State the blood parasite species.
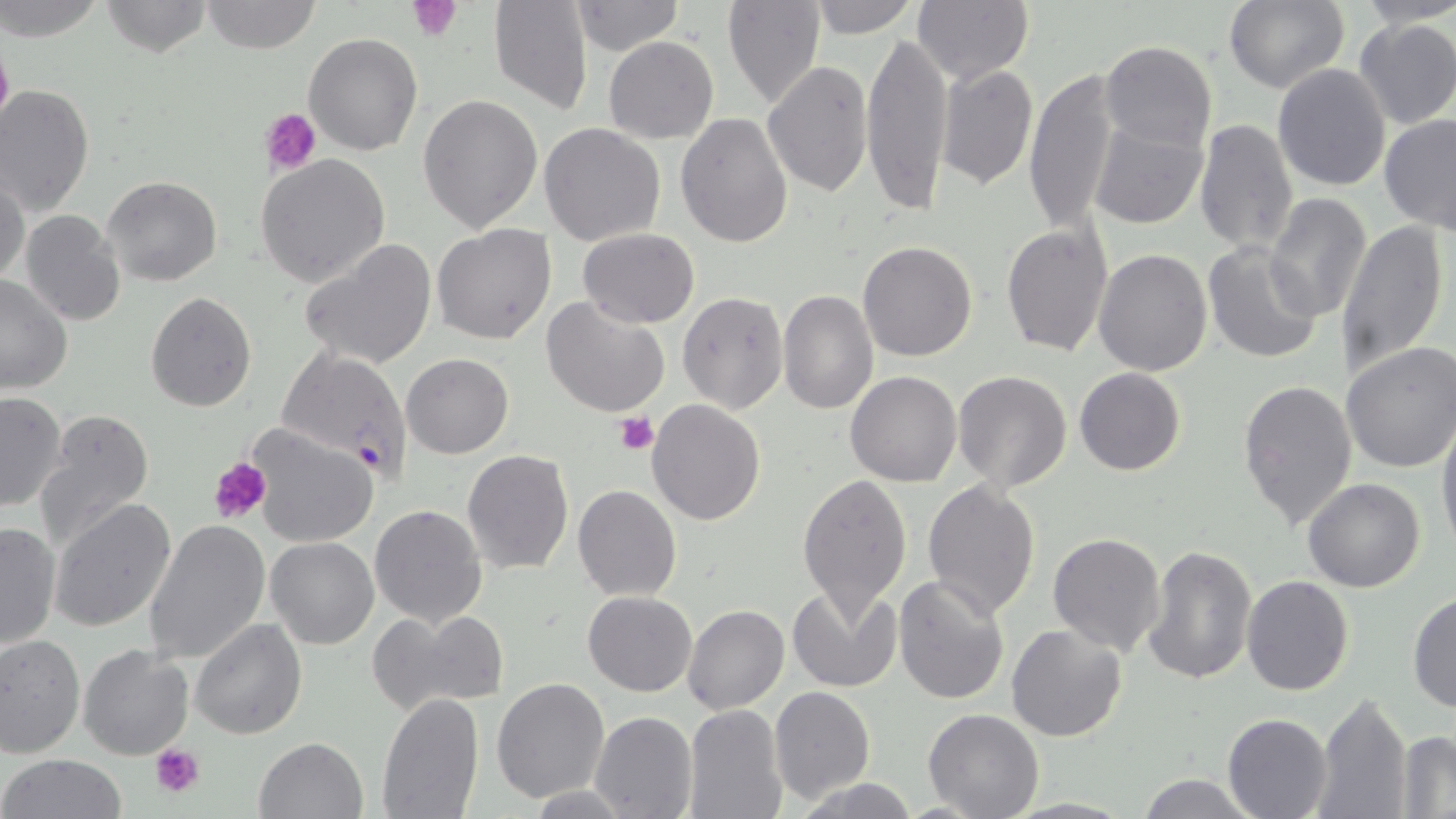

Plasmodium falciparum.

platelet locations = approximate bounding boxes as (x1,y1)-(x2,y2) corner pairs in pixels: (409,1)-(465,41), (261,108)-(321,176), (614,412)-(658,456), (208,456)-(272,526), (150,744)-(204,798)
image size = 1456×819 pixels
preparation = thin blood smear
magnification = 1000x
Plasmodium falciparum-infected red blood cell locations = approximate bounding boxes as (x1,y1)-(x2,y2) corner pairs in pixels: (277,346)-(412,478)
field of view = single
stain = May-Grünwald-Giemsa
uninfected red blood cell locations = approximate bounding boxes as (x1,y1)-(x2,y2) corner pairs in pixels: (0,0)-(106,41), (200,0)-(322,53), (487,0)-(595,114), (722,0)-(825,110), (805,0)-(921,36), (912,0)-(1033,85), (1224,0)-(1349,95), (98,1)-(215,56), (1352,1)-(1456,30), (570,2)-(683,56), (1353,16)-(1456,129), (860,25)-(952,221), (304,32)-(422,156), (604,36)-(719,144), (1099,40)-(1217,153), (761,60)-(873,197), (937,63)-(1037,191), (1272,64)-(1393,192), (1024,68)-(1119,237), (0,84)-(94,218), (418,93)-(543,232), (418,110)-(668,238), (676,113)-(794,249), (1380,113)-(1456,233), (1194,118)-(1298,255), (1088,119)-(1209,230), (540,122)-(667,246), (256,155)-(390,288), (0,172)-(28,284), (102,175)-(222,287), (1264,194)-(1370,322), (21,210)-(125,327), (1336,218)-(1448,378), (1002,222)-(1110,358), (431,223)-(557,345), (576,228)-(699,327), (300,240)-(438,371), (858,241)-(978,362), (1202,241)-(1323,364), (1094,250)-(1213,376), (0,273)-(73,393), (778,289)-(877,414), (145,291)-(257,412), (677,291)-(789,414), (540,296)-(671,421), (1340,343)-(1456,473), (401,353)-(514,458), (1075,368)-(1186,476), (845,370)-(962,487), (953,371)-(1073,493), (1236,378)-(1358,529), (0,391)-(67,512), (646,399)-(766,524), (34,410)-(156,552), (1436,419)-(1456,557), (248,426)-(377,547), (462,449)-(574,573), (795,473)-(912,618), (1303,476)-(1426,593), (922,479)-(1040,620), (573,485)-(680,600), (49,498)-(177,633), (370,504)-(487,626), (145,520)-(271,666), (0,521)-(61,650), (1048,532)-(1166,655), (265,538)-(379,650), (1141,543)-(1256,687), (893,573)-(1010,706), (1241,574)-(1354,695), (790,585)-(901,695), (583,591)-(696,697), (1408,593)-(1456,711), (683,604)-(790,715), (369,608)-(511,716), (190,617)-(307,738), (1006,623)-(1128,743), (0,633)-(84,758), (79,645)-(195,761), (492,678)-(609,803), (769,686)-(877,804), (376,692)-(483,819), (1315,693)-(1412,819), (682,702)-(789,819), (923,709)-(1044,819), (590,711)-(697,819), (1223,713)-(1332,819), (1394,733)-(1456,816), (253,736)-(367,819), (1,754)-(128,819), (1135,772)-(1262,819), (794,778)-(924,817)
modality = optical microscopy